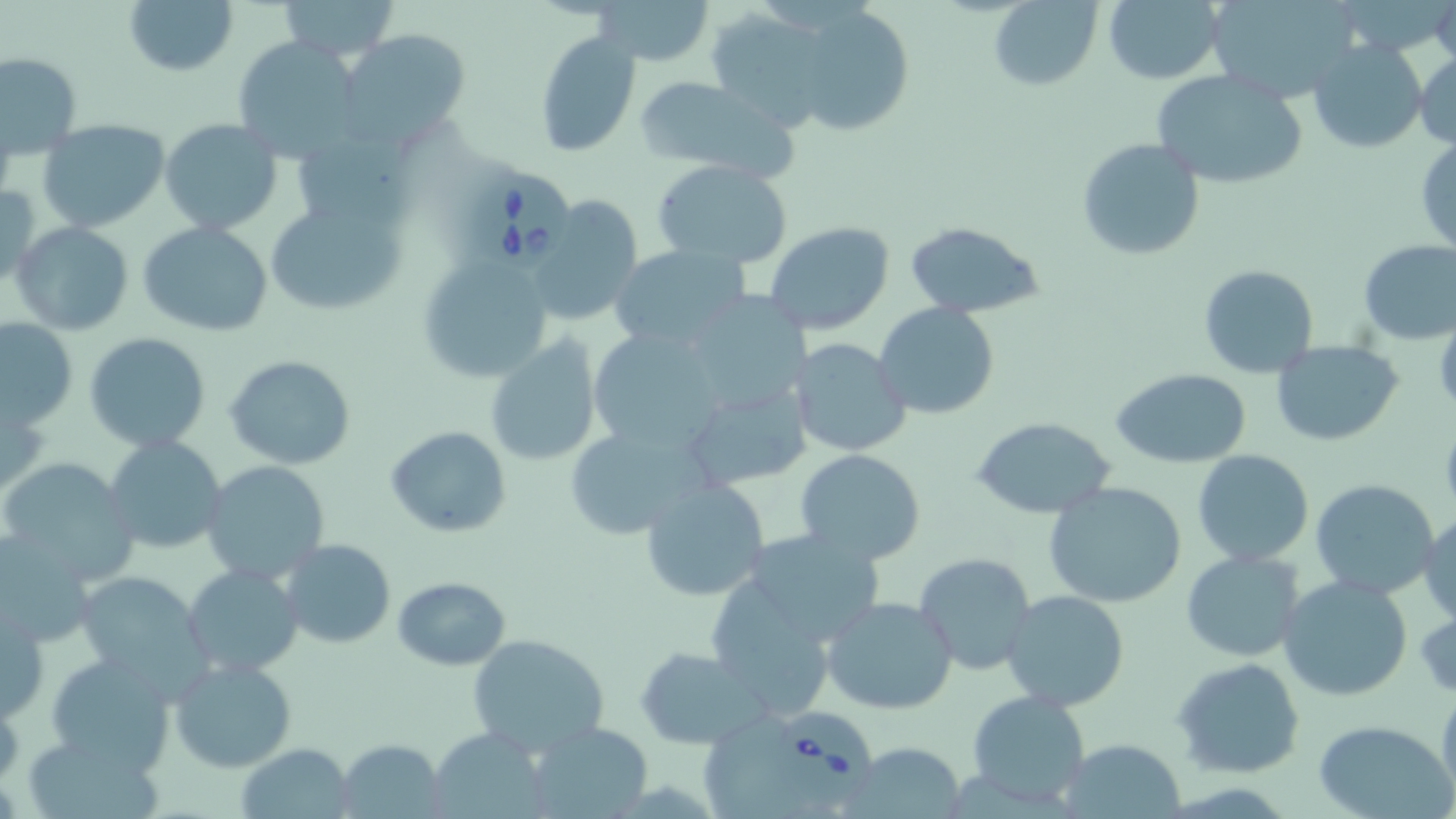
Summary:
  - Coordinate format: approximate bounding boxes as (x1, y1, x2, y2) in pixels
  - Babesia divergens-infected red blood cell locations: (469, 169, 574, 270), (772, 704, 881, 810)
  - Uninfected red blood cell locations: (123, 0, 238, 75), (277, 0, 400, 61), (596, 0, 713, 66), (988, 0, 1101, 90), (1101, 0, 1225, 84), (1204, 0, 1363, 104), (787, 3, 913, 134), (339, 29, 471, 147), (534, 32, 641, 157), (231, 35, 367, 160), (1307, 39, 1427, 155), (1413, 49, 1456, 149), (1, 52, 81, 158), (1151, 68, 1308, 190), (634, 78, 796, 181), (295, 118, 419, 226), (160, 119, 284, 236), (37, 120, 170, 233), (1076, 137, 1205, 262), (1415, 138, 1456, 259), (650, 159, 794, 267), (0, 181, 41, 287), (529, 193, 643, 327), (263, 195, 410, 315), (903, 220, 1044, 318), (10, 221, 135, 335), (138, 221, 273, 337), (764, 222, 895, 335), (1358, 237, 1456, 343), (610, 245, 750, 351), (418, 253, 555, 381), (1198, 264, 1318, 379), (691, 295, 807, 412), (874, 302, 999, 420), (0, 319, 76, 430), (586, 326, 728, 450), (83, 332, 211, 452), (483, 337, 603, 466), (789, 337, 913, 457), (1270, 340, 1403, 447), (225, 356, 355, 469), (1113, 369, 1253, 470), (681, 380, 812, 494), (971, 417, 1118, 519), (562, 422, 709, 541), (386, 426, 512, 536), (105, 435, 227, 557), (1192, 449, 1313, 566), (795, 450, 926, 564), (2, 458, 140, 580), (201, 459, 331, 584), (639, 479, 770, 603), (1310, 479, 1441, 601), (1043, 481, 1188, 608), (1418, 512, 1456, 626), (739, 527, 889, 645), (0, 533, 99, 650), (279, 540, 397, 649), (1179, 551, 1306, 661), (914, 552, 1039, 676), (184, 563, 304, 677), (75, 573, 210, 686), (392, 576, 510, 670), (1277, 576, 1413, 703), (1002, 590, 1132, 711), (822, 596, 957, 715), (1, 602, 47, 723), (467, 634, 608, 754), (635, 646, 769, 749), (44, 652, 177, 772), (169, 656, 298, 772), (1173, 657, 1306, 778), (1437, 680, 1456, 809), (969, 690, 1090, 808), (1312, 719, 1455, 819), (528, 725, 652, 814), (425, 727, 551, 819), (24, 728, 168, 819), (337, 738, 446, 816), (1059, 738, 1185, 817), (842, 741, 966, 818), (233, 742, 357, 818)
  - Slide-level diagnosis: Babesia divergens
  - Magnification: 1000x
  - Field of view: single
  - Stain: May-Grünwald-Giemsa
  - Image size: 1456×819 pixels
  - Preparation: thin blood smear
  - Modality: optical microscopy